State which cell type is depicted.
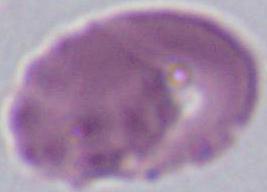

An erythrocyte.

{
  "modality": "photomicrograph",
  "magnification": "1000x"
}